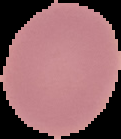
{
  "preparation": "thin blood film",
  "malaria_status": "uninfected",
  "image_size": "121×139 pixels",
  "image_type": "segmented cell region on a black background"
}